Point out each Plasmodium parasite.
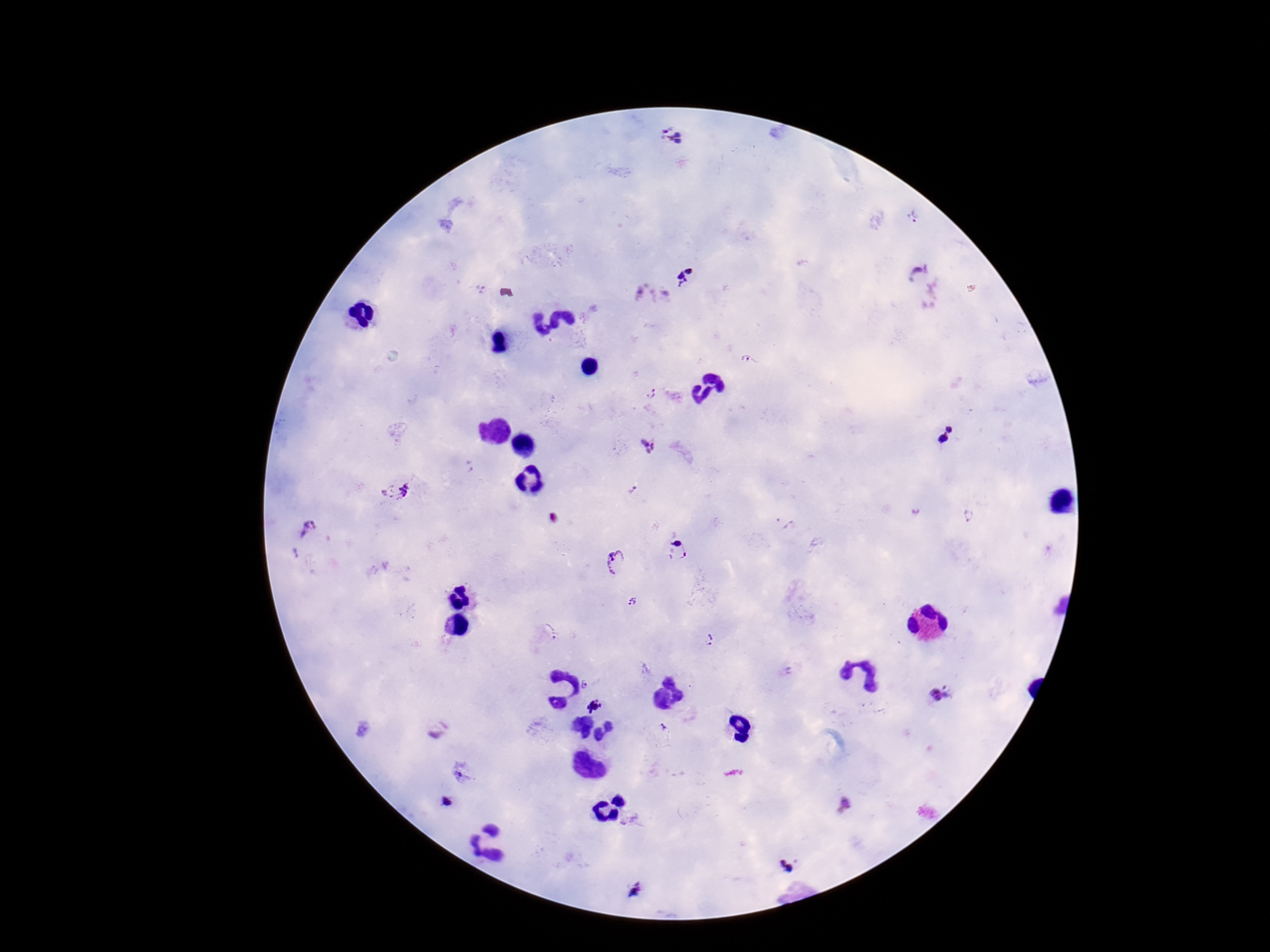
Approximate centers as [x, y] in pixels.
Plasmodium parasites: [670, 137], [915, 217], [687, 279], [748, 361], [649, 394], [944, 433], [647, 447], [632, 489], [396, 491], [970, 515], [782, 524], [308, 528], [678, 550], [616, 562], [632, 601], [544, 634], [709, 639], [586, 683], [941, 695], [595, 707], [664, 730], [447, 802], [787, 867], [635, 891].

Smartphone photograph taken through the microscope eyepiece. Patient malaria status: infected. One field from this slide. Image is 1270×952 pixels. 100x magnification. Thick peripheral-blood smear. Giemsa-stained preparation.